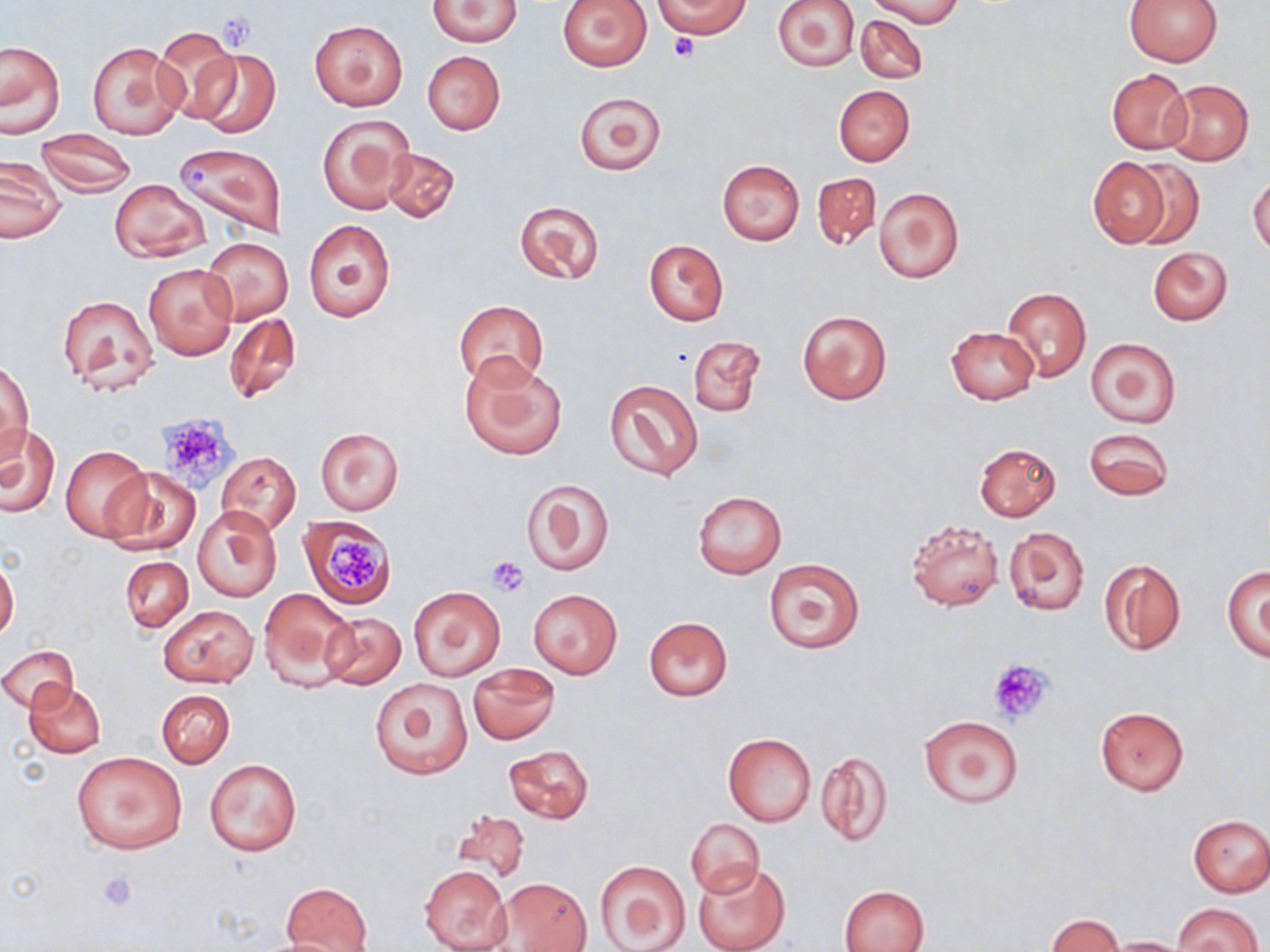 Approximate bounding boxes as (x1,y1)-(x2,y2) corner pairs in pixels. Platelet locations: (670,33)-(699,62), (156,415)-(239,491), (324,529)-(388,592), (486,555)-(530,596), (986,657)-(1056,725), (98,870)-(138,911). Uninfected red blood cell locations: (425,0)-(522,46), (655,0)-(751,38), (772,0)-(861,71), (868,0)-(964,26), (1123,0)-(1224,66), (557,1)-(651,71), (856,14)-(927,83), (309,19)-(408,111), (154,26)-(244,122), (1,40)-(65,136), (87,41)-(187,140), (190,47)-(282,139), (422,51)-(505,134), (1106,68)-(1192,155), (1163,80)-(1254,165), (834,85)-(915,165), (574,91)-(665,175), (317,113)-(415,214), (36,131)-(136,195), (172,142)-(286,238), (380,146)-(460,224), (0,157)-(65,244), (1087,157)-(1173,248), (718,159)-(805,245), (1127,161)-(1204,247), (812,172)-(881,252), (1248,174)-(1270,255), (110,178)-(209,262), (874,186)-(964,283), (514,199)-(604,286), (304,219)-(395,323), (201,237)-(294,325), (644,240)-(729,325), (1148,247)-(1232,325), (144,262)-(238,361), (1002,287)-(1091,381), (57,294)-(160,397), (454,300)-(549,390), (797,308)-(893,405), (224,312)-(301,405), (945,326)-(1039,405), (688,336)-(766,418), (1086,337)-(1181,428), (460,354)-(567,461), (1,360)-(32,461), (604,379)-(703,482), (0,424)-(59,518), (316,426)-(404,515), (1083,427)-(1173,501), (974,442)-(1060,522), (61,445)-(152,541), (216,451)-(300,533), (102,468)-(201,555), (520,477)-(615,575), (692,491)-(786,578), (193,506)-(281,602), (300,514)-(396,609), (905,519)-(1004,613), (1005,526)-(1090,615), (0,556)-(18,643), (120,556)-(193,631), (1098,557)-(1186,655), (764,558)-(865,655), (1222,566)-(1270,659), (408,586)-(505,680), (258,587)-(356,689), (529,589)-(622,678), (159,604)-(258,687), (318,611)-(407,690), (643,616)-(734,701), (1,645)-(78,713), (468,663)-(559,743), (369,677)-(473,780), (23,681)-(106,758), (157,690)-(234,767), (1094,706)-(1190,794), (919,715)-(1024,807), (722,732)-(816,826), (503,744)-(594,825), (816,749)-(894,847), (72,752)-(189,854), (205,758)-(301,855), (454,806)-(532,885), (1187,815)-(1270,896), (686,817)-(764,898), (594,860)-(692,951), (693,860)-(790,952), (419,865)-(510,951), (493,877)-(591,951), (281,883)-(372,951), (840,885)-(930,952), (1172,902)-(1262,951), (1046,914)-(1122,951), (257,935)-(361,952), (1104,936)-(1190,951). Slide-level diagnosis: no evidence of blood parasites. Image is 1270×952 pixels. May-Grünwald-Giemsa-stained preparation. Light microscopy. Thin blood film. Captured at 1000x magnification. Single field of view.